Locate every Plasmodium ovale-infected red blood cell.
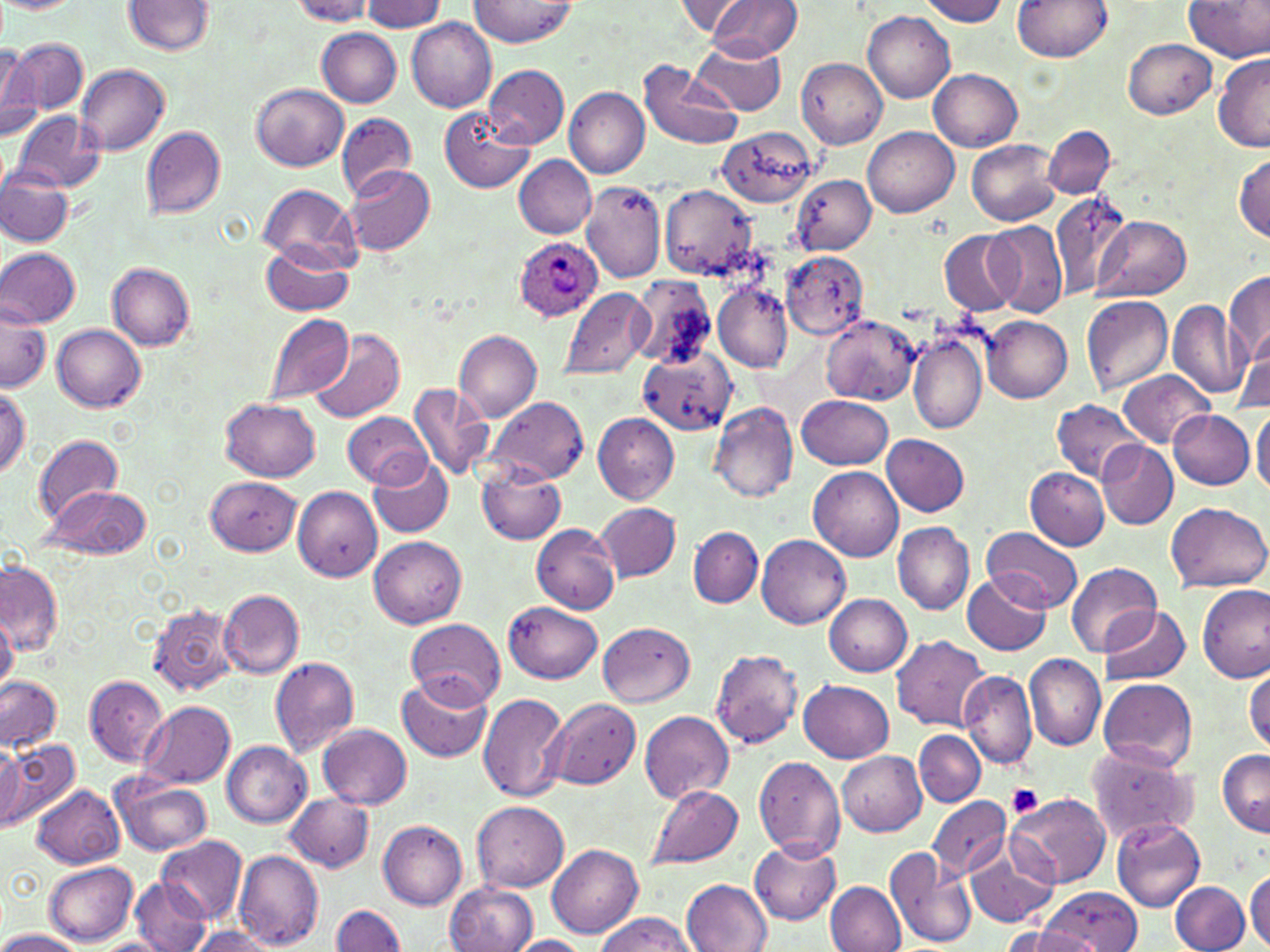

Approximate bounding boxes as [x1, y1, x2, y2] in pixels.
Plasmodium ovale-infected red blood cells: [513, 237, 602, 322].

slide-level diagnosis = Plasmodium ovale
uninfected red blood cell locations = approximate bounding boxes as [x1, y1, x2, y2] in pixels: [289, 0, 377, 24], [471, 0, 575, 47], [708, 0, 802, 59], [919, 0, 1009, 25], [1014, 0, 1111, 61], [1185, 0, 1269, 61], [0, 1, 81, 12], [123, 1, 213, 54], [359, 1, 446, 32], [676, 1, 755, 40], [864, 12, 953, 103], [405, 18, 496, 113], [318, 29, 402, 107], [691, 37, 786, 115], [3, 38, 87, 114], [1124, 38, 1217, 118], [0, 44, 42, 142], [1212, 55, 1270, 152], [797, 58, 888, 148], [639, 59, 742, 150], [75, 63, 170, 155], [484, 64, 569, 148], [928, 67, 1022, 150], [252, 85, 348, 171], [565, 88, 650, 177], [441, 105, 534, 193], [11, 112, 104, 192], [336, 112, 417, 200], [139, 125, 226, 219], [863, 125, 958, 217], [1044, 125, 1115, 198], [723, 128, 826, 213], [967, 139, 1062, 226], [514, 154, 597, 237], [1233, 155, 1269, 241], [346, 166, 436, 256], [1, 169, 74, 246], [792, 175, 876, 254], [580, 182, 666, 281], [258, 185, 359, 266], [661, 185, 759, 278], [1047, 192, 1136, 299], [1093, 215, 1190, 301], [984, 220, 1068, 318], [940, 231, 1020, 317], [261, 243, 354, 316], [0, 249, 80, 328], [780, 250, 870, 340], [107, 262, 195, 350], [1224, 271, 1270, 366], [629, 276, 720, 370], [714, 283, 793, 372], [560, 287, 653, 381], [1081, 295, 1173, 394], [0, 298, 49, 395], [1167, 301, 1250, 400], [263, 312, 355, 406], [821, 315, 920, 404], [983, 315, 1073, 403], [53, 325, 146, 413], [455, 330, 543, 421], [909, 330, 989, 435], [309, 331, 405, 424], [1230, 347, 1270, 413], [643, 351, 737, 436], [1117, 371, 1215, 447], [0, 383, 29, 479], [408, 383, 496, 481], [799, 395, 894, 469], [485, 397, 589, 483], [222, 398, 321, 481], [1052, 401, 1145, 482], [709, 403, 799, 502], [1251, 407, 1270, 497], [1168, 410, 1256, 489], [343, 411, 431, 487], [594, 413, 679, 503], [33, 434, 122, 524], [881, 434, 969, 515], [1098, 441, 1177, 530], [369, 457, 452, 537], [477, 463, 566, 545], [807, 465, 903, 561], [1026, 468, 1110, 549], [206, 476, 302, 555], [40, 484, 151, 559], [292, 486, 383, 582], [1167, 502, 1268, 591], [595, 503, 681, 580], [892, 521, 974, 614], [532, 523, 622, 613], [688, 527, 762, 607], [982, 527, 1082, 612], [756, 534, 849, 627], [369, 536, 466, 628], [0, 560, 61, 657], [1067, 562, 1162, 659], [962, 572, 1050, 657], [1197, 583, 1269, 682], [217, 589, 304, 679], [824, 594, 912, 675], [503, 601, 602, 683], [147, 603, 238, 696], [1100, 605, 1191, 685], [0, 610, 17, 694], [405, 618, 505, 708], [597, 623, 696, 707], [891, 635, 989, 731], [709, 648, 803, 750], [1023, 654, 1104, 751], [269, 657, 359, 757], [1245, 668, 1270, 753], [959, 670, 1036, 769], [396, 674, 493, 762], [0, 676, 61, 751], [83, 676, 168, 767], [1098, 677, 1197, 772], [800, 679, 894, 762], [478, 693, 569, 802], [548, 697, 641, 788], [137, 700, 235, 789], [639, 710, 734, 803], [318, 724, 411, 809], [914, 730, 985, 807], [1, 739, 81, 829], [221, 740, 312, 828], [0, 743, 26, 830], [1085, 743, 1200, 842], [1217, 748, 1270, 835], [836, 750, 927, 835], [754, 757, 846, 860], [110, 774, 213, 857], [645, 783, 744, 871], [32, 784, 124, 868], [284, 793, 374, 873], [1008, 793, 1110, 888], [928, 795, 1010, 880], [471, 800, 569, 892], [1110, 816, 1206, 912], [378, 820, 467, 909], [158, 835, 247, 922], [749, 839, 841, 925], [965, 839, 1059, 928], [547, 844, 643, 939], [884, 846, 976, 950], [234, 850, 323, 949], [44, 859, 138, 944], [1246, 869, 1270, 948], [129, 877, 212, 952], [682, 879, 771, 951], [444, 881, 536, 952], [826, 881, 906, 951], [1170, 881, 1250, 952], [1036, 888, 1144, 949], [331, 904, 405, 951], [594, 913, 695, 952], [1000, 925, 1089, 952], [187, 926, 278, 952], [0, 928, 85, 952], [507, 935, 591, 952], [94, 938, 168, 952]
preparation = thin blood film
platelet locations = approximate bounding boxes as [x1, y1, x2, y2] in pixels: [1008, 784, 1043, 817]
modality = light microscopy
field of view = single
image size = 1270×952 pixels
magnification = 1000x
stain = May-Grünwald-Giemsa